State which cell type is depicted.
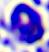
A leukocyte.

modality = micrograph
magnification = 400x